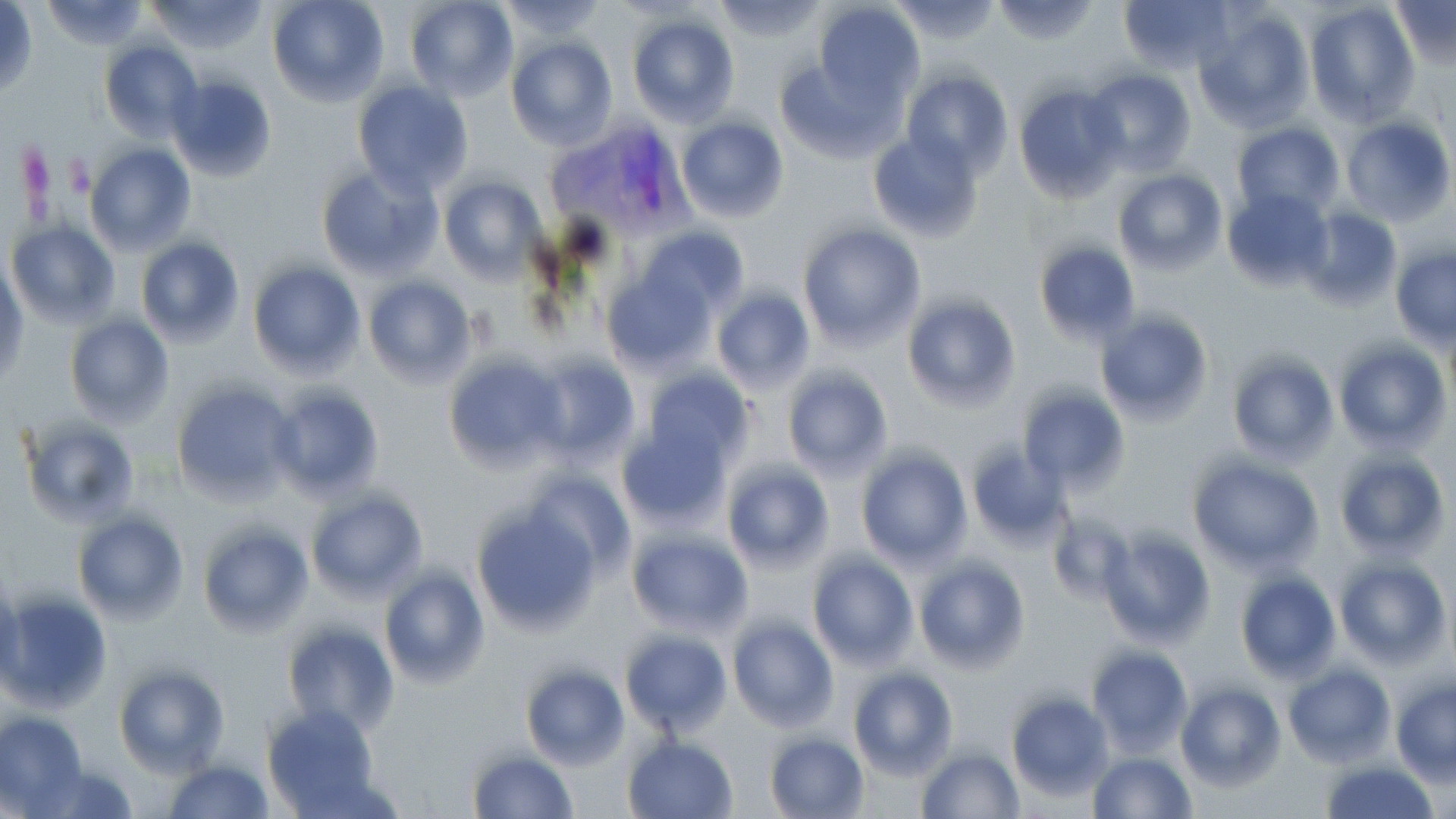 Approximate bounding boxes as (x1,y1)-(x2,y2) corner pairs in pixels. Plasmodium vivax-infected red blood cell locations: (548,118)-(690,234). Uninfected red blood cell locations: (40,0)-(149,50), (147,0)-(269,54), (267,0)-(389,107), (404,0)-(518,103), (501,0)-(608,40), (711,0)-(825,42), (889,0)-(1003,44), (988,0)-(1102,46), (1119,0)-(1235,75), (812,1)-(924,105), (1304,2)-(1419,125), (1388,2)-(1455,70), (0,3)-(39,100), (1195,7)-(1314,134), (625,11)-(739,125), (506,38)-(616,150), (98,40)-(201,142), (774,58)-(901,164), (1084,67)-(1197,175), (901,68)-(1013,176), (167,73)-(276,182), (351,81)-(474,197), (1012,85)-(1127,201), (675,115)-(789,223), (1340,116)-(1455,227), (1230,123)-(1344,221), (867,129)-(984,242), (84,143)-(195,254), (318,165)-(441,281), (1113,169)-(1226,276), (438,175)-(547,285), (1225,179)-(1335,296), (1301,205)-(1401,312), (6,219)-(120,328), (796,223)-(925,351), (639,225)-(749,317), (137,234)-(245,347), (1034,239)-(1140,348), (1391,246)-(1456,348), (248,261)-(364,379), (0,263)-(28,384), (600,269)-(715,376), (363,276)-(477,388), (712,287)-(816,395), (902,294)-(1020,410), (1094,306)-(1214,428), (65,313)-(174,428), (1333,338)-(1450,454), (1227,351)-(1340,465), (442,354)-(569,475), (532,354)-(640,466), (779,365)-(894,481), (639,367)-(755,472), (172,380)-(297,503), (266,384)-(385,501), (1018,386)-(1129,494), (19,415)-(140,527), (616,421)-(736,531), (967,443)-(1073,544), (1334,448)-(1449,560), (857,449)-(971,567), (1189,458)-(1324,572), (723,461)-(834,574), (524,471)-(635,578), (306,490)-(428,604), (471,503)-(598,635), (73,511)-(188,626), (1046,511)-(1134,608), (198,522)-(313,638), (1098,527)-(1216,647), (625,530)-(751,636), (807,553)-(918,670), (913,556)-(1030,674), (1335,559)-(1450,668), (378,564)-(489,688), (1235,570)-(1341,683), (1,579)-(25,690), (1,593)-(112,712), (728,617)-(838,732), (282,622)-(398,737), (620,629)-(732,738), (1088,644)-(1193,756), (1020,656)-(1149,785), (519,661)-(628,769), (1282,661)-(1394,767), (115,665)-(229,776), (848,668)-(958,779), (1391,677)-(1456,785), (1175,682)-(1285,792), (1007,691)-(1114,802), (261,704)-(383,814), (0,710)-(87,812), (765,730)-(870,817), (623,736)-(738,819), (914,744)-(1024,819), (467,747)-(578,818), (1087,750)-(1196,818), (163,757)-(272,818), (1321,759)-(1437,819), (29,763)-(140,819). Slide-level diagnosis: Plasmodium vivax. May-Grünwald-Giemsa-stained preparation. Optical microscopy. Captured at 1000x magnification. Image is 1456×819 pixels. Thin blood film. Single field of view.